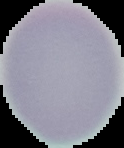

Summary:
  - Image size: 124×148 pixels
  - Image type: cell region segmented out of the field of view; surrounding area masked to black
  - Preparation: thin blood smear
  - Malaria status: uninfected